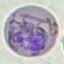
Summary:
  - Result: malaria parasites detected
  - Image type: automatically extracted cell patch, resized to 64 × 64 pixels
  - Capture: smartphone through the microscope eyepiece
  - Preparation: thin blood smear
  - Stain: Giemsa